Identify the parasite.
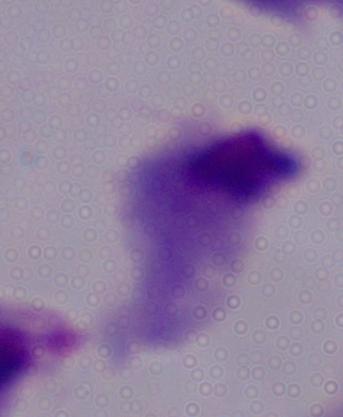

This is a trichomonad.

Captured at 1000x magnification. Micrograph.